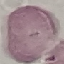
Malaria status: uninfected. Photographed with a smartphone camera at the microscope eyepiece. Giemsa-stained preparation. Cell patch, automatically extracted from a larger field of view and resized to 64 × 64 pixels. Thin blood film.